Identify the blood parasite species.
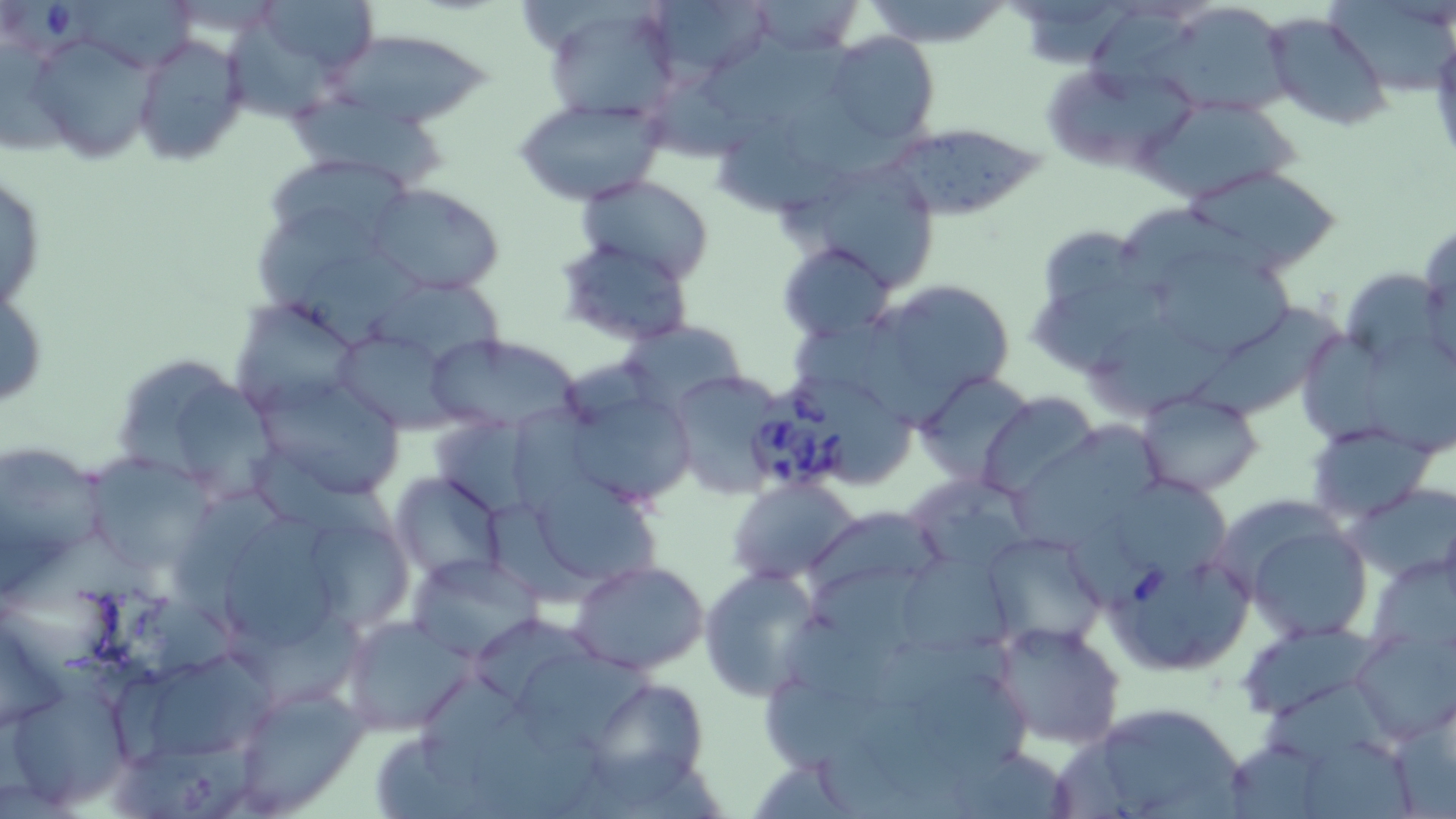
Babesia divergens.

Summary:
  - Coordinate format: approximate bounding boxes as named x1/y1/x2/y2 corners in pixels
  - Uninfected red blood cell locations: (x1=248, y1=0, x2=383, y2=86), (x1=643, y1=0, x2=774, y2=86), (x1=862, y1=0, x2=1012, y2=49), (x1=749, y1=2, x2=864, y2=55), (x1=537, y1=3, x2=678, y2=124), (x1=1150, y1=8, x2=1295, y2=118), (x1=221, y1=10, x2=351, y2=126), (x1=1265, y1=12, x2=1392, y2=131), (x1=25, y1=28, x2=165, y2=165), (x1=332, y1=28, x2=491, y2=126), (x1=132, y1=32, x2=249, y2=166), (x1=825, y1=32, x2=939, y2=149), (x1=1045, y1=70, x2=1201, y2=169), (x1=512, y1=96, x2=666, y2=206), (x1=287, y1=97, x2=461, y2=197), (x1=1143, y1=97, x2=1295, y2=204), (x1=717, y1=116, x2=882, y2=213), (x1=877, y1=132, x2=1050, y2=217), (x1=262, y1=152, x2=415, y2=262), (x1=782, y1=158, x2=945, y2=295), (x1=1184, y1=166, x2=1343, y2=271), (x1=1, y1=169, x2=47, y2=316), (x1=574, y1=175, x2=716, y2=280), (x1=366, y1=182, x2=507, y2=296), (x1=1111, y1=203, x2=1291, y2=301), (x1=1419, y1=235, x2=1456, y2=369), (x1=777, y1=241, x2=896, y2=343), (x1=559, y1=243, x2=699, y2=345), (x1=1161, y1=264, x2=1295, y2=355), (x1=1344, y1=269, x2=1446, y2=369), (x1=368, y1=272, x2=510, y2=376), (x1=0, y1=275, x2=48, y2=420), (x1=1027, y1=279, x2=1193, y2=370), (x1=864, y1=298, x2=975, y2=437), (x1=233, y1=299, x2=366, y2=416), (x1=1197, y1=307, x2=1354, y2=419), (x1=618, y1=320, x2=744, y2=414), (x1=1088, y1=320, x2=1253, y2=419), (x1=329, y1=328, x2=457, y2=432), (x1=1304, y1=328, x2=1412, y2=449), (x1=423, y1=333, x2=582, y2=435), (x1=1365, y1=334, x2=1456, y2=462), (x1=107, y1=350, x2=273, y2=497), (x1=663, y1=370, x2=787, y2=498), (x1=916, y1=372, x2=1037, y2=487), (x1=254, y1=375, x2=408, y2=502), (x1=557, y1=381, x2=697, y2=509), (x1=978, y1=393, x2=1102, y2=498), (x1=1138, y1=393, x2=1264, y2=496), (x1=1016, y1=419, x2=1164, y2=556), (x1=1307, y1=423, x2=1431, y2=523), (x1=0, y1=446, x2=118, y2=560), (x1=86, y1=459, x2=218, y2=574), (x1=390, y1=471, x2=508, y2=581), (x1=908, y1=472, x2=1039, y2=578), (x1=1122, y1=475, x2=1235, y2=581), (x1=728, y1=478, x2=859, y2=582), (x1=538, y1=479, x2=671, y2=589), (x1=1350, y1=483, x2=1455, y2=580), (x1=178, y1=491, x2=297, y2=624), (x1=802, y1=506, x2=949, y2=605), (x1=1235, y1=516, x2=1372, y2=641), (x1=218, y1=519, x2=345, y2=653), (x1=318, y1=522, x2=422, y2=638), (x1=977, y1=530, x2=1107, y2=653), (x1=406, y1=553, x2=543, y2=661), (x1=903, y1=556, x2=1014, y2=658), (x1=1370, y1=556, x2=1453, y2=653), (x1=571, y1=561, x2=709, y2=674), (x1=699, y1=566, x2=823, y2=701), (x1=339, y1=615, x2=474, y2=736), (x1=988, y1=621, x2=1126, y2=750), (x1=1239, y1=622, x2=1384, y2=721), (x1=1351, y1=632, x2=1456, y2=743), (x1=513, y1=648, x2=660, y2=745), (x1=146, y1=655, x2=277, y2=763), (x1=6, y1=673, x2=135, y2=813), (x1=913, y1=673, x2=1043, y2=779), (x1=230, y1=682, x2=369, y2=814), (x1=596, y1=683, x2=710, y2=805), (x1=1262, y1=686, x2=1395, y2=775), (x1=1068, y1=698, x2=1249, y2=819), (x1=467, y1=706, x2=601, y2=819), (x1=372, y1=729, x2=502, y2=819), (x1=1300, y1=736, x2=1422, y2=819)
  - Babesia divergens-infected red blood cell locations: (x1=12, y1=1, x2=113, y2=61), (x1=745, y1=387, x2=859, y2=493), (x1=1111, y1=553, x2=1254, y2=674)
  - Image size: 1456×819 pixels
  - Modality: light microscopy
  - Magnification: 1000x
  - Field of view: single
  - Preparation: thin blood smear
  - Stain: May-Grünwald-Giemsa